Name the cell type shown.
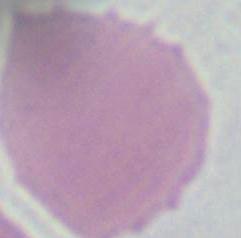

An erythrocyte.

Summary:
  - Magnification: 1000x
  - Modality: micrograph